Report the malaria status of this cell.
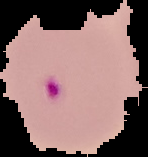

It is parasitized.

image type = segmented cell region with the area outside set to black
preparation = thin blood film
image size = 148×157 pixels